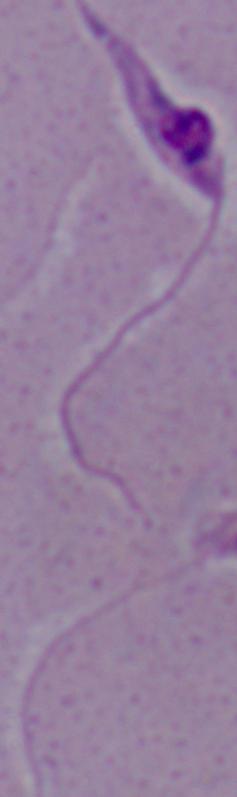 A Leishmania parasite is seen. 1000x magnification. Micrograph.